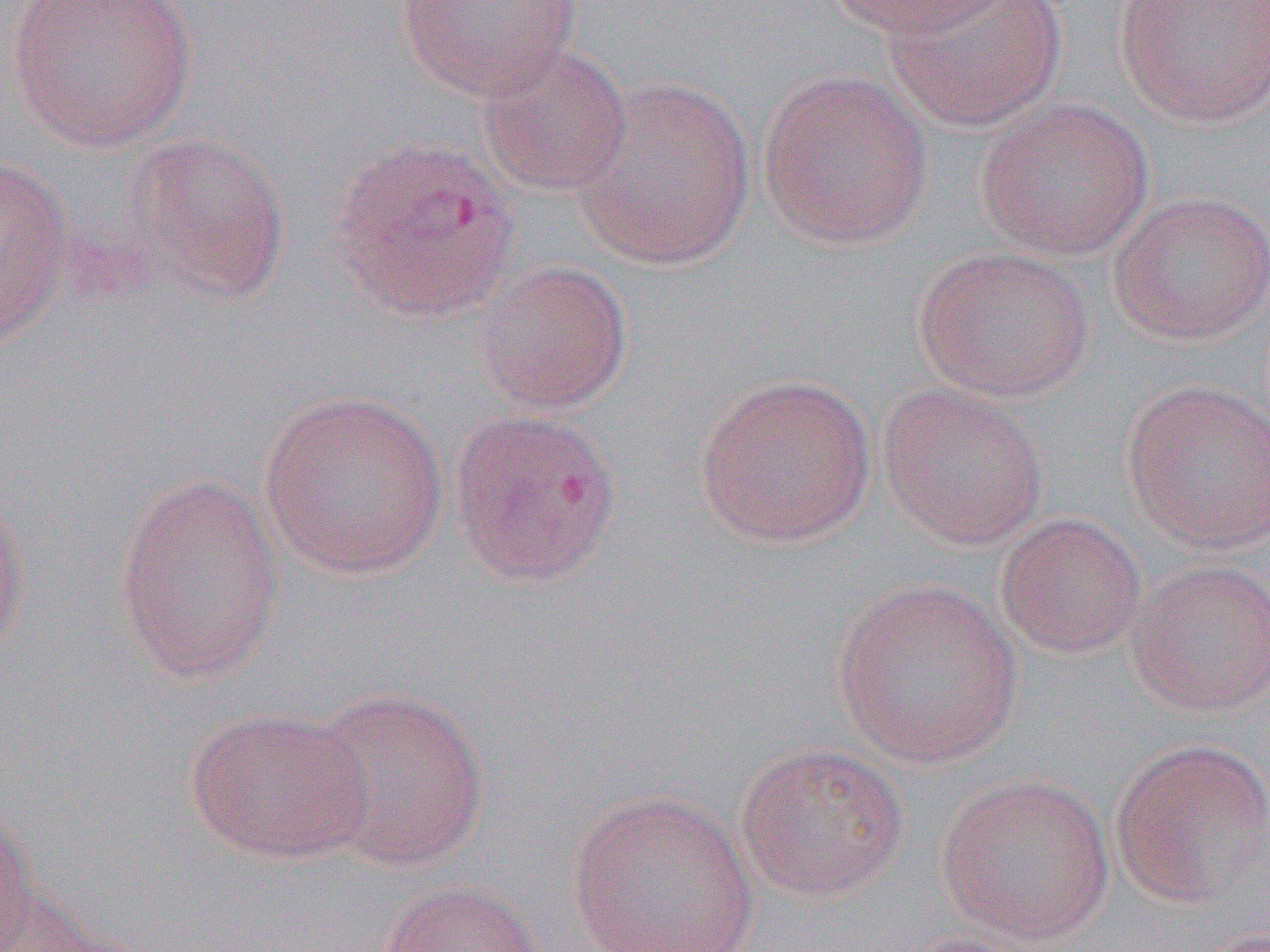

slide-level diagnosis = Plasmodium vivax
image size = 1270×952 pixels
uninfected red blood cell locations = approximate bounding boxes as named x1/y1/x2/y2 corners in pixels: (x1=7, y1=0, x2=198, y2=152), (x1=824, y1=0, x2=1008, y2=41), (x1=886, y1=0, x2=1066, y2=132), (x1=1113, y1=0, x2=1269, y2=129), (x1=395, y1=1, x2=582, y2=100), (x1=474, y1=43, x2=632, y2=197), (x1=756, y1=68, x2=935, y2=251), (x1=574, y1=75, x2=757, y2=269), (x1=974, y1=97, x2=1154, y2=260), (x1=119, y1=131, x2=292, y2=306), (x1=330, y1=134, x2=522, y2=323), (x1=0, y1=155, x2=73, y2=350), (x1=1106, y1=191, x2=1270, y2=347), (x1=914, y1=243, x2=1095, y2=404), (x1=472, y1=259, x2=633, y2=415), (x1=693, y1=373, x2=878, y2=549), (x1=1122, y1=379, x2=1270, y2=553), (x1=877, y1=383, x2=1050, y2=549), (x1=257, y1=388, x2=450, y2=580), (x1=448, y1=406, x2=624, y2=588), (x1=112, y1=472, x2=285, y2=686), (x1=0, y1=490, x2=31, y2=674), (x1=995, y1=512, x2=1148, y2=660), (x1=1126, y1=558, x2=1270, y2=716), (x1=831, y1=577, x2=1025, y2=768), (x1=302, y1=684, x2=491, y2=873), (x1=184, y1=706, x2=376, y2=865), (x1=1109, y1=738, x2=1270, y2=907), (x1=734, y1=740, x2=909, y2=903), (x1=934, y1=771, x2=1116, y2=946), (x1=565, y1=788, x2=761, y2=952), (x1=0, y1=804, x2=37, y2=952), (x1=374, y1=880, x2=548, y2=952), (x1=1, y1=898, x2=153, y2=952)
magnification = 1000x
preparation = thin blood film
field of view = one of a larger specimen
modality = light microscopy